Draw a bounding box around every leukocyte (white blood cell).
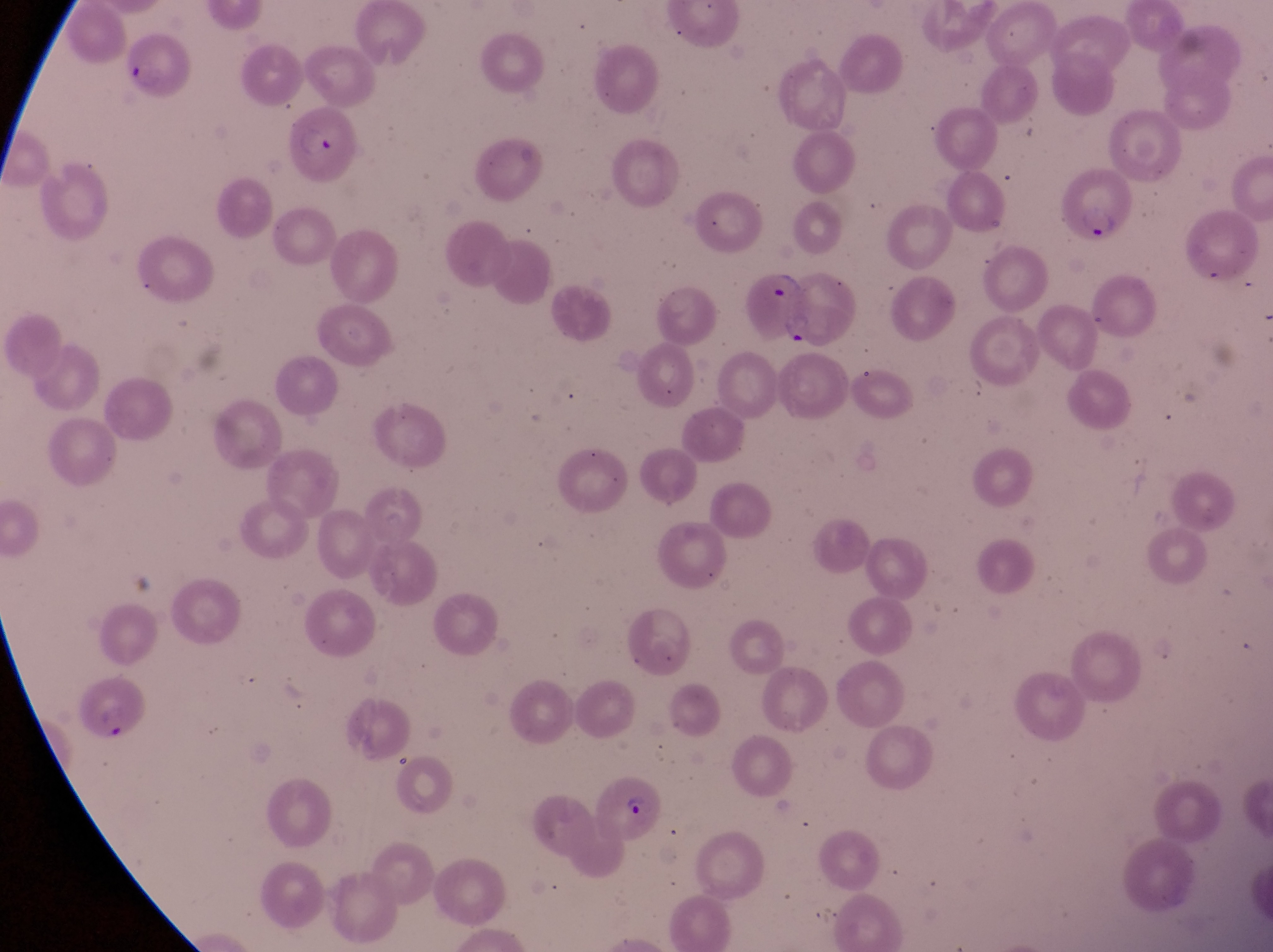

No leukocytes observed.

trophozoite locations = approximate bounding boxes as [left, top, right, bottom] in pixels: [769, 270, 806, 303], [781, 309, 818, 349]
field of view = single
magnification = 1000x
image size = 1273×952 pixels
parasitised red blood cell locations = approximate bounding boxes as [left, top, right, bottom] in pixels: [120, 39, 190, 101], [285, 108, 363, 190], [1063, 170, 1132, 244], [74, 669, 146, 744], [597, 776, 664, 838]
capture = smartphone photograph through the eyepiece of an Olympus CX-23 microscope
preparation = thin blood smear
country = Uganda